Classify this cell by malaria status.
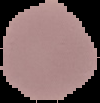
It is uninfected.

From a thin blood film. Image is 100×103 pixels. Segmented cell region on a black background.